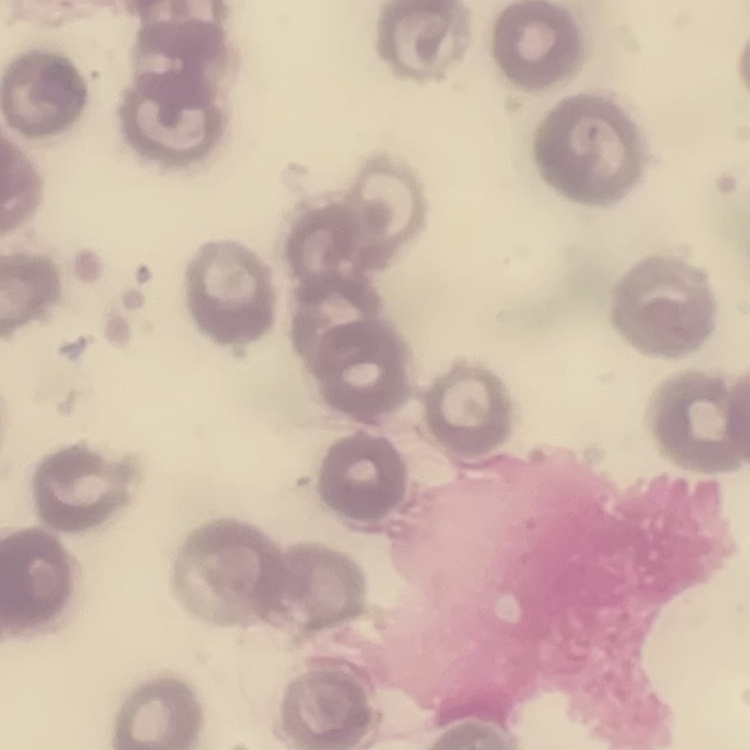

The erythrocytes show no rouleaux formation. Square crop of a larger photomicrograph. Field's or Giemsa stain. Thin blood smear.